Outline platelets.
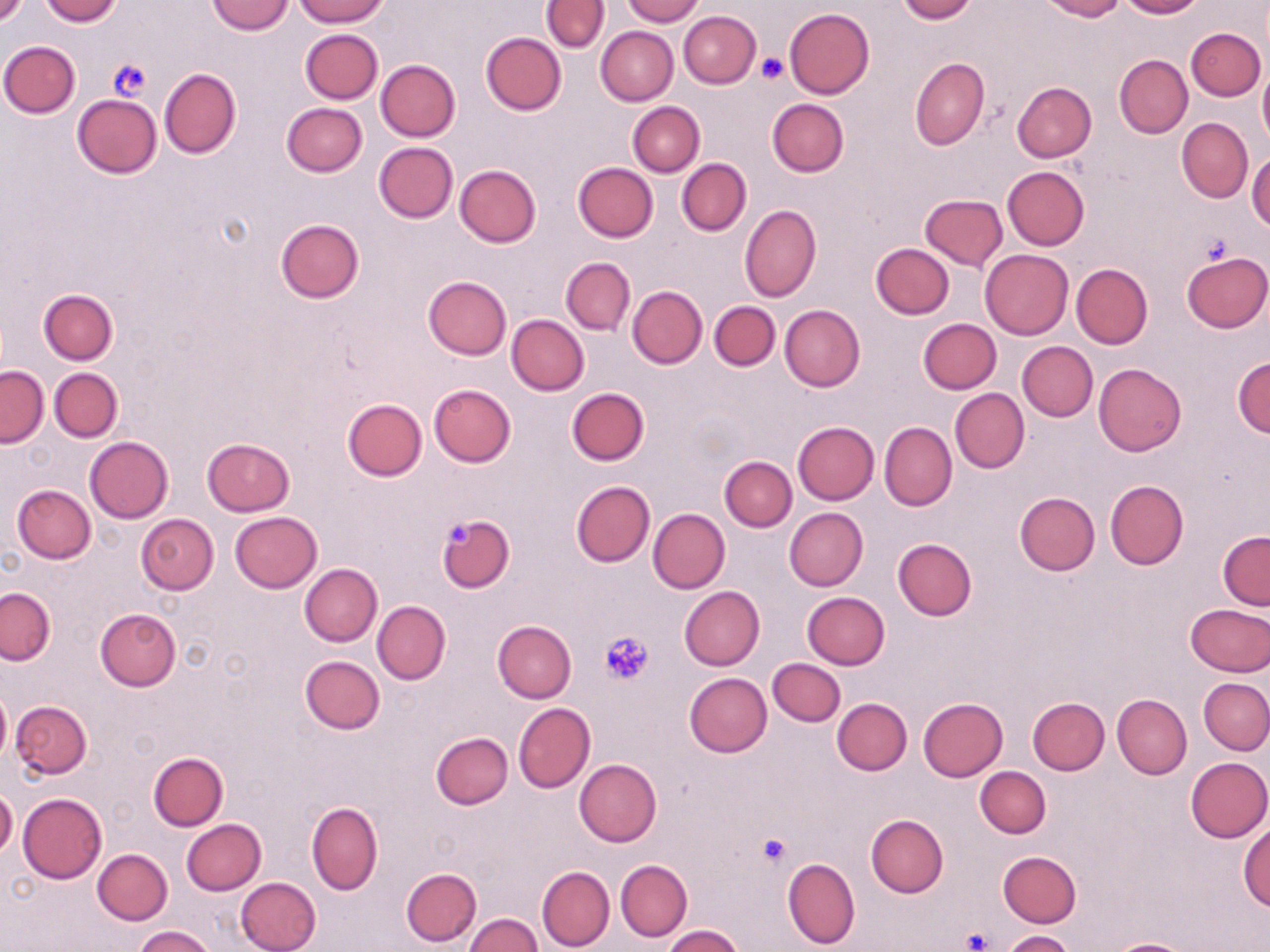

Approximate bounding boxes as named x1/y1/x2/y2 corners in pixels.
Platelets: (x1=757, y1=53, x2=789, y2=83), (x1=108, y1=58, x2=151, y2=102), (x1=1200, y1=235, x2=1232, y2=265), (x1=446, y1=519, x2=477, y2=549), (x1=600, y1=631, x2=654, y2=686), (x1=755, y1=833, x2=791, y2=868), (x1=962, y1=928, x2=991, y2=951).

Uninfected red blood cell locations: (x1=0, y1=0, x2=28, y2=26), (x1=40, y1=0, x2=122, y2=25), (x1=207, y1=0, x2=295, y2=35), (x1=293, y1=0, x2=389, y2=26), (x1=623, y1=0, x2=703, y2=25), (x1=897, y1=0, x2=977, y2=23), (x1=1039, y1=0, x2=1124, y2=21), (x1=1117, y1=0, x2=1204, y2=19), (x1=541, y1=1, x2=608, y2=52), (x1=785, y1=8, x2=874, y2=99), (x1=678, y1=10, x2=761, y2=88), (x1=596, y1=26, x2=677, y2=106), (x1=1188, y1=27, x2=1265, y2=100), (x1=300, y1=29, x2=382, y2=104), (x1=292, y1=30, x2=373, y2=174), (x1=479, y1=32, x2=566, y2=116), (x1=1, y1=40, x2=81, y2=118), (x1=1114, y1=54, x2=1193, y2=139), (x1=909, y1=57, x2=988, y2=151), (x1=375, y1=59, x2=460, y2=142), (x1=1259, y1=66, x2=1270, y2=146), (x1=159, y1=67, x2=241, y2=159), (x1=1011, y1=81, x2=1097, y2=162), (x1=71, y1=94, x2=162, y2=179), (x1=766, y1=99, x2=849, y2=177), (x1=628, y1=102, x2=704, y2=176), (x1=281, y1=103, x2=367, y2=177), (x1=1177, y1=118, x2=1253, y2=203), (x1=374, y1=142, x2=458, y2=223), (x1=1248, y1=153, x2=1270, y2=232), (x1=677, y1=158, x2=750, y2=236), (x1=454, y1=163, x2=541, y2=247), (x1=572, y1=163, x2=658, y2=242), (x1=1002, y1=167, x2=1089, y2=251), (x1=920, y1=194, x2=1008, y2=271), (x1=740, y1=204, x2=822, y2=302), (x1=275, y1=218, x2=365, y2=304), (x1=870, y1=243, x2=955, y2=319), (x1=980, y1=248, x2=1073, y2=340), (x1=1182, y1=250, x2=1269, y2=333), (x1=561, y1=257, x2=635, y2=334), (x1=1071, y1=264, x2=1152, y2=349), (x1=422, y1=276, x2=510, y2=361), (x1=627, y1=286, x2=706, y2=369), (x1=38, y1=290, x2=118, y2=365), (x1=709, y1=301, x2=780, y2=371), (x1=780, y1=304, x2=865, y2=391), (x1=506, y1=314, x2=589, y2=396), (x1=917, y1=318, x2=1001, y2=394), (x1=1017, y1=341, x2=1098, y2=421), (x1=1233, y1=356, x2=1270, y2=437), (x1=1093, y1=363, x2=1186, y2=455), (x1=0, y1=365, x2=48, y2=447), (x1=49, y1=368, x2=123, y2=442), (x1=428, y1=383, x2=516, y2=467), (x1=567, y1=387, x2=650, y2=466), (x1=950, y1=388, x2=1029, y2=473), (x1=343, y1=398, x2=428, y2=481), (x1=792, y1=421, x2=879, y2=504), (x1=879, y1=422, x2=956, y2=511), (x1=85, y1=437, x2=173, y2=523), (x1=202, y1=438, x2=296, y2=515), (x1=719, y1=457, x2=796, y2=532), (x1=1105, y1=479, x2=1188, y2=569), (x1=571, y1=480, x2=655, y2=568), (x1=12, y1=485, x2=95, y2=564), (x1=1014, y1=492, x2=1100, y2=575), (x1=647, y1=508, x2=730, y2=593), (x1=784, y1=508, x2=869, y2=591), (x1=230, y1=511, x2=322, y2=593), (x1=136, y1=514, x2=218, y2=594), (x1=437, y1=514, x2=515, y2=594), (x1=1217, y1=531, x2=1269, y2=610), (x1=892, y1=539, x2=976, y2=621), (x1=299, y1=563, x2=382, y2=646), (x1=678, y1=586, x2=765, y2=671), (x1=0, y1=588, x2=54, y2=665), (x1=802, y1=592, x2=890, y2=669), (x1=372, y1=600, x2=450, y2=685), (x1=1186, y1=603, x2=1270, y2=677), (x1=96, y1=608, x2=181, y2=692), (x1=492, y1=621, x2=576, y2=702), (x1=299, y1=656, x2=384, y2=734), (x1=766, y1=658, x2=845, y2=727), (x1=684, y1=673, x2=771, y2=756), (x1=1199, y1=679, x2=1270, y2=755), (x1=0, y1=691, x2=11, y2=763), (x1=1113, y1=693, x2=1192, y2=778), (x1=1026, y1=696, x2=1109, y2=775), (x1=832, y1=698, x2=912, y2=775), (x1=918, y1=698, x2=1007, y2=780), (x1=11, y1=700, x2=91, y2=777), (x1=513, y1=702, x2=596, y2=792), (x1=431, y1=732, x2=513, y2=810), (x1=148, y1=751, x2=227, y2=830), (x1=1184, y1=756, x2=1270, y2=842), (x1=574, y1=759, x2=662, y2=847), (x1=975, y1=766, x2=1051, y2=838), (x1=0, y1=788, x2=17, y2=859), (x1=17, y1=793, x2=107, y2=883), (x1=306, y1=801, x2=383, y2=894), (x1=866, y1=814, x2=949, y2=897), (x1=181, y1=819, x2=266, y2=895), (x1=1239, y1=821, x2=1269, y2=910), (x1=93, y1=848, x2=173, y2=924), (x1=997, y1=850, x2=1082, y2=927), (x1=781, y1=857, x2=860, y2=950), (x1=616, y1=859, x2=692, y2=941), (x1=537, y1=866, x2=615, y2=950), (x1=400, y1=868, x2=481, y2=947), (x1=235, y1=877, x2=322, y2=952), (x1=466, y1=913, x2=543, y2=951), (x1=662, y1=925, x2=743, y2=952), (x1=133, y1=926, x2=215, y2=952), (x1=1002, y1=929, x2=1074, y2=952), (x1=1104, y1=938, x2=1197, y2=952). Slide-level diagnosis: negative for blood parasites. Thin blood film. Optical microscopy. Image is 1270×952 pixels. Single field of view. 1000x magnification. May-Grünwald-Giemsa stain.